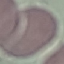 Malaria status: uninfected. Automatically extracted cell patch, resized to 64 × 64 pixels. Giemsa stain. Thin blood film. Photographed with a smartphone camera at the microscope eyepiece.